Give the position of every leukocyte.
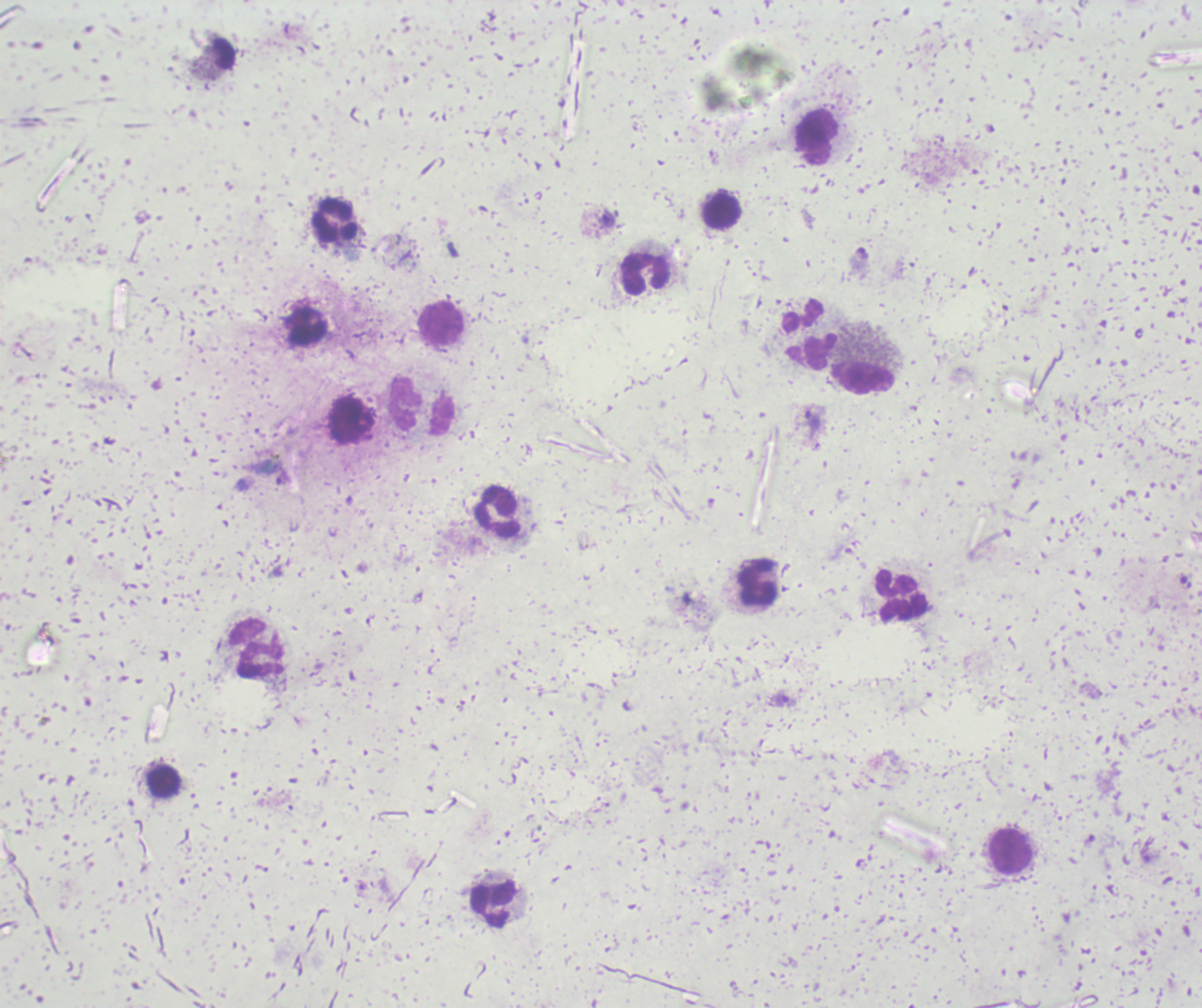

Approximate object centers, in pixels from the top-left corner.
Leukocytes: (x=816, y=136), (x=720, y=211), (x=333, y=220), (x=644, y=273), (x=441, y=323), (x=305, y=326), (x=807, y=333), (x=862, y=379), (x=422, y=406), (x=498, y=510), (x=757, y=583), (x=901, y=596), (x=257, y=647), (x=164, y=781), (x=1010, y=851), (x=493, y=905).

Approximate object centers, in pixels from the top-left corner.
Summary:
  - Trophozoite locations: (x=606, y=218), (x=858, y=258), (x=810, y=424), (x=283, y=478), (x=783, y=699)
  - Image size: 1202×1008 pixels
  - Context: previously used in a real diagnosis
  - Background quality: unsatisfactory
  - Magnification: 100x
  - Stain: Romanowsky
  - Result: malaria parasites detected
  - Field of view: single
  - Preparation: thick blood smear